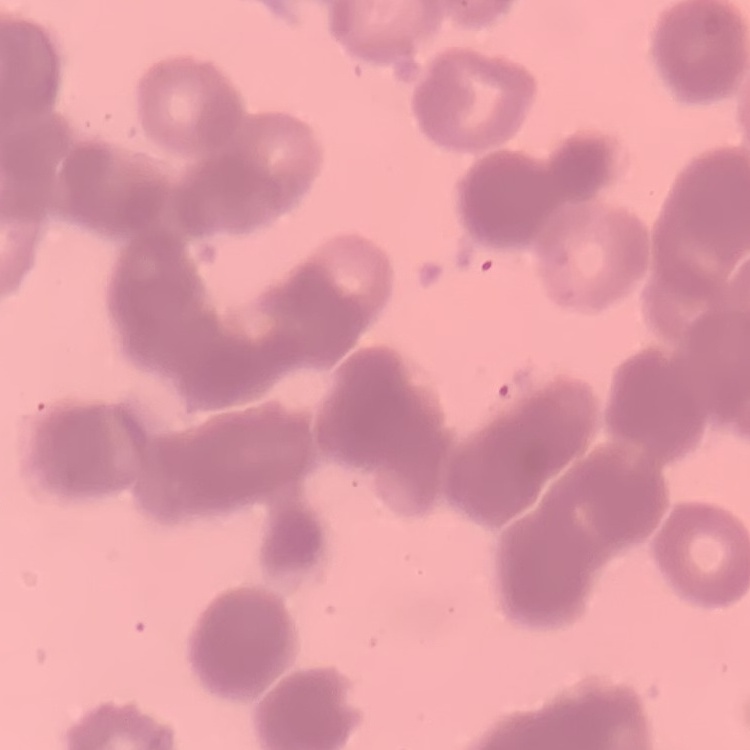
Summary:
  - Erythrocyte morphology: rouleaux formation
  - Preparation: thin peripheral smear
  - Stain: Field's or Giemsa
  - Image type: square crop of a larger photomicrograph